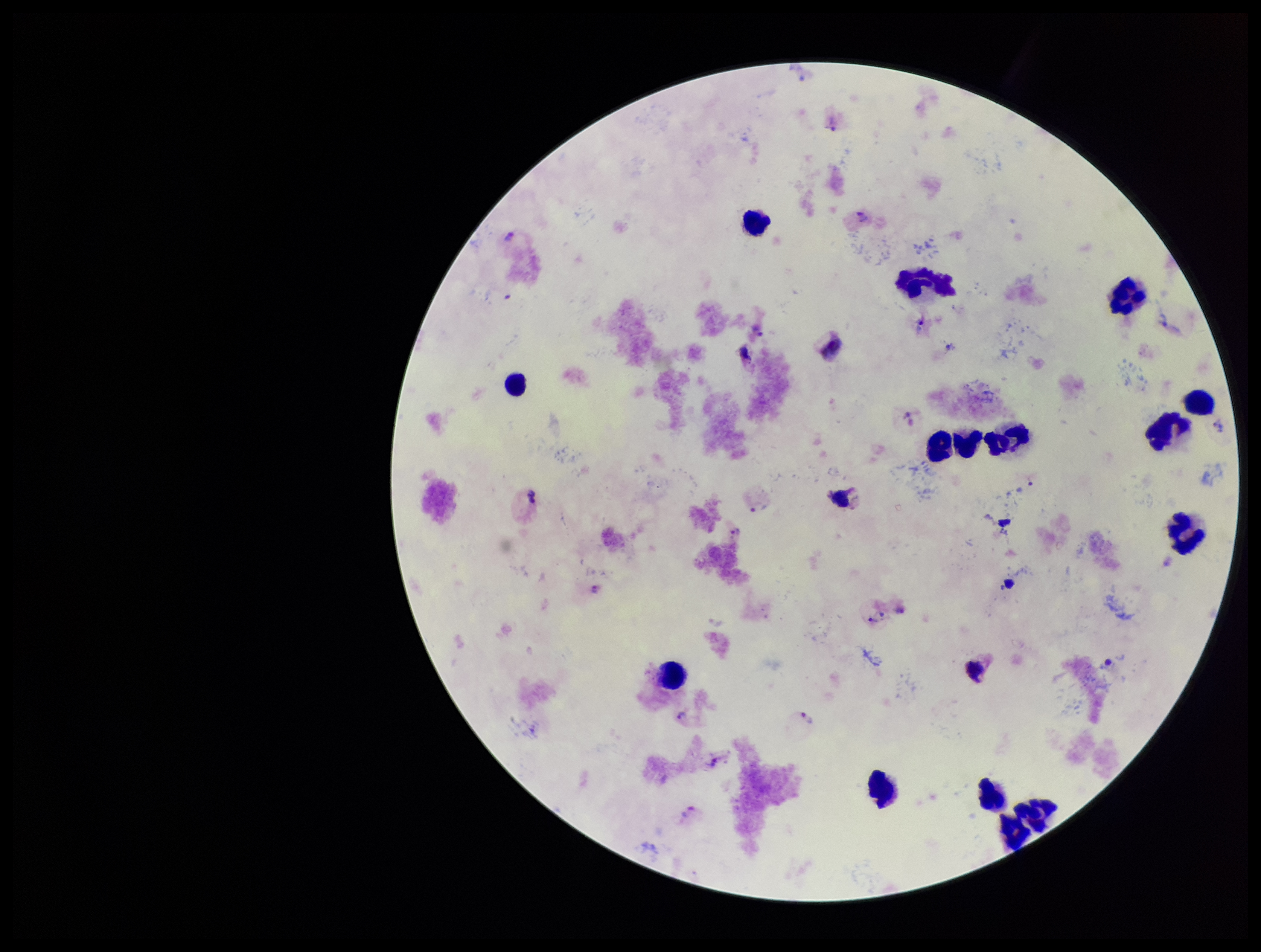
leukocyte count = 15
Plasmodium parasites = detected
species reported for this patient = Plasmodium vivax
field of view = single
patient malaria status = infected
stain = Giemsa
capture = smartphone photograph through the microscope eyepiece
preparation = thick
parasite count = 12
image size = 1261×952 pixels